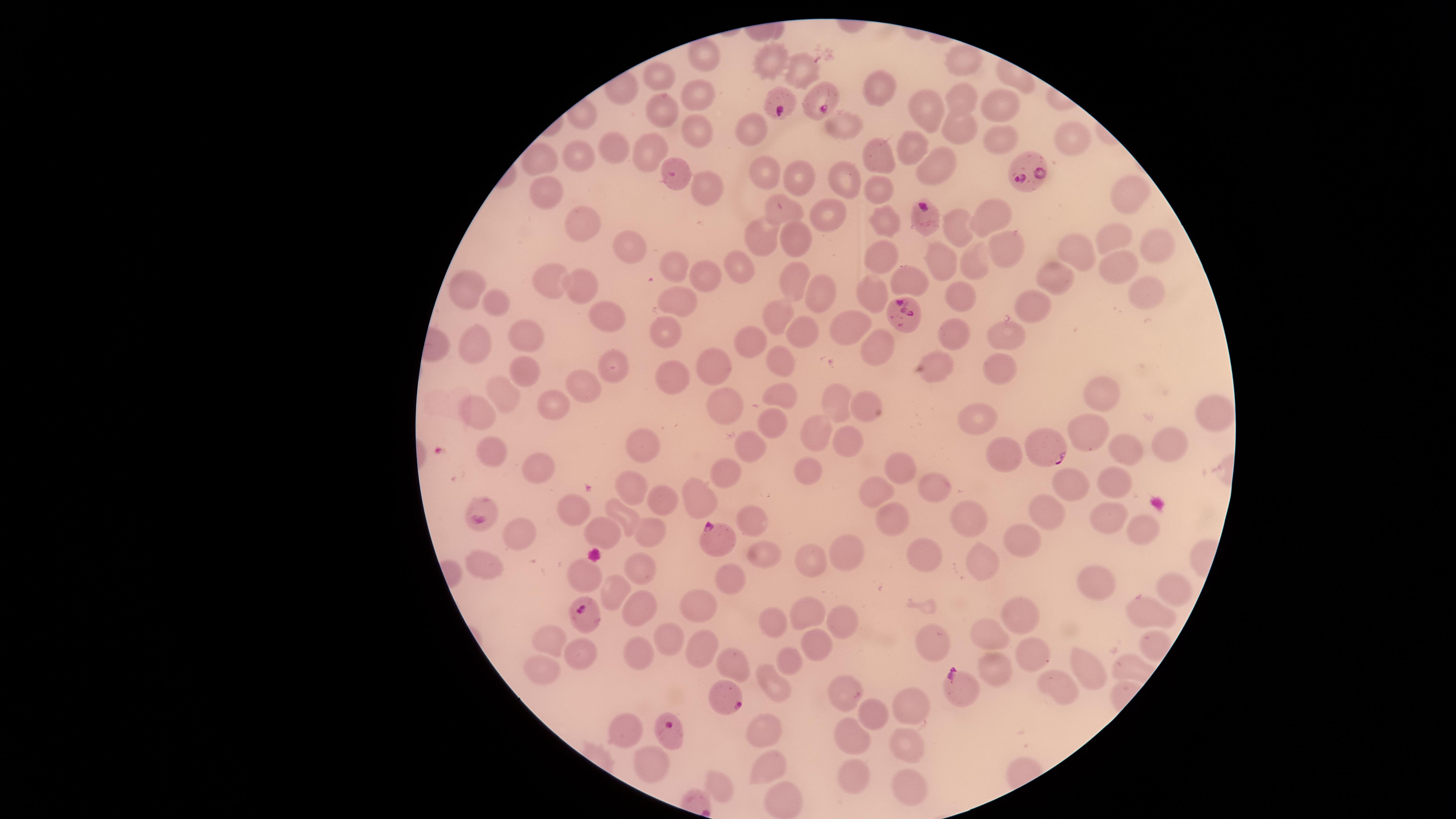
uninfected RBCs = approximate marker points as (x, y) in pixels: (700, 52), (962, 57), (779, 67), (803, 70), (664, 73), (875, 86), (959, 95), (697, 96), (926, 110), (998, 112), (657, 113), (749, 127), (954, 127), (843, 128), (695, 135), (1072, 139), (997, 145), (621, 147), (908, 148), (648, 153), (579, 154), (880, 156), (537, 160), (934, 169), (764, 174), (805, 179), (844, 182), (704, 183), (545, 189), (876, 190), (1123, 194), (785, 209), (822, 213), (989, 215), (883, 219), (577, 222), (955, 225), (762, 238), (1117, 239), (799, 240), (624, 243), (1158, 243), (1005, 248), (880, 252), (1082, 252), (937, 259), (978, 262), (1114, 263), (670, 267), (731, 267), (1050, 273), (904, 275), (708, 276), (791, 281), (545, 282), (581, 282), (465, 289), (1148, 289), (813, 292), (878, 292), (955, 295), (678, 296), (1038, 303), (491, 304), (603, 315), (779, 317), (841, 327), (671, 330), (1005, 331), (806, 332), (523, 333), (951, 335), (749, 342), (478, 346), (882, 348), (784, 359), (522, 364), (714, 366), (1001, 367), (610, 368), (936, 370), (677, 380), (583, 386), (507, 391), (776, 396), (1105, 397), (839, 402), (725, 404), (865, 406), (551, 411), (474, 412), (1210, 414), (979, 422), (770, 426), (1088, 435), (817, 438), (851, 443), (1166, 445), (638, 449), (493, 450), (1127, 450), (749, 452), (1003, 454), (906, 465), (527, 466), (728, 471), (814, 472), (1113, 482), (1069, 484), (935, 485), (631, 488), (878, 495), (701, 497), (662, 501), (575, 506), (896, 514), (971, 515), (625, 516), (1044, 516), (1107, 517), (751, 520), (1133, 525), (604, 531), (648, 533), (517, 537), (1023, 540), (926, 549), (847, 550), (762, 553), (978, 555), (816, 562), (488, 565), (645, 568), (580, 574), (734, 579), (1104, 586), (1174, 589), (616, 592), (636, 604), (706, 606), (1014, 613), (1152, 613), (808, 614), (769, 621), (840, 621), (985, 632), (666, 633), (815, 638), (544, 639), (931, 642), (1155, 644), (699, 645), (575, 651), (636, 651), (1028, 655), (785, 658), (733, 663), (542, 668), (1082, 671), (995, 672), (775, 684), (847, 687), (1059, 687), (909, 705), (871, 708), (626, 731), (765, 731), (853, 736), (909, 740), (652, 762), (768, 765), (856, 769), (716, 778), (908, 783), (778, 802)
image size = 1456×819 pixels
preparation = thin blood film
capture = smartphone photograph through the microscope eyepiece
visible region = circular
field of view = single
stain = Giemsa
presence = malaria parasites identified
species = Plasmodium falciparum
parasitized RBCs = approximate marker points as (x, y) in pixels: (819, 94), (773, 101), (1026, 170), (676, 173), (920, 213), (902, 309), (1043, 446), (482, 513), (711, 536), (581, 610), (952, 682), (727, 691), (670, 729)